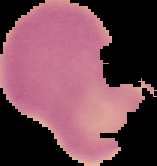

Summary:
  - Malaria status: uninfected
  - Preparation: thin blood film
  - Image type: cell region segmented out of the field of view; surrounding area masked to black
  - Image size: 157×166 pixels